Assess this cell for malaria.
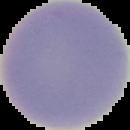
Uninfected.

{
  "image_type": "segmented cell region with the area outside set to black",
  "image_size": "130×130 pixels",
  "preparation": "thin blood smear"
}